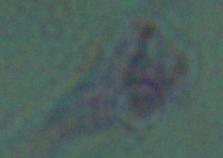
Captured at 1000x magnification. A Leishmania parasite is shown. Micrograph.